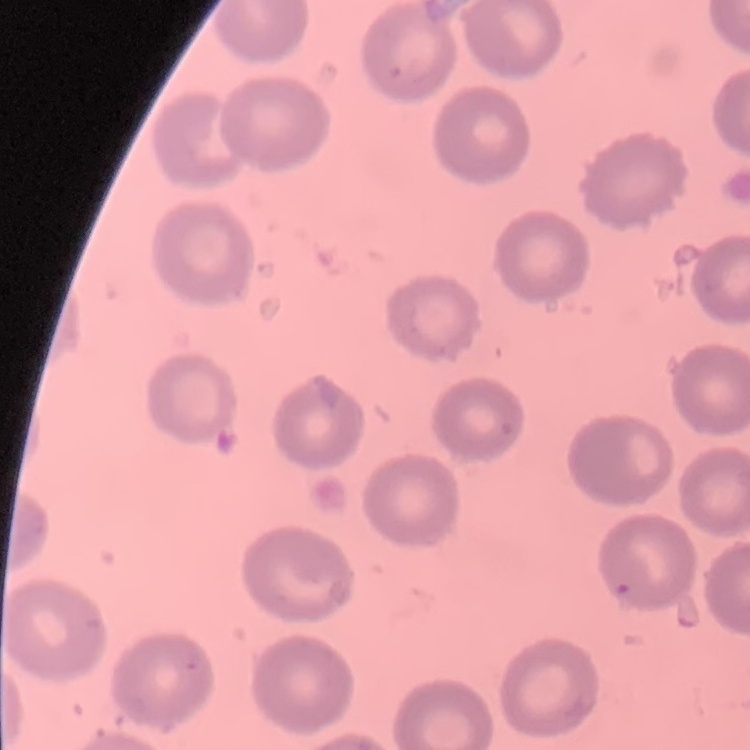

erythrocyte morphology = no rouleaux formation
image type = one tile cut from a larger photomicrograph
preparation = thin blood smear
stain = Field's or Giemsa